State which parasite is depicted.
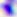
Toxoplasma gondii.

Summary:
  - Magnification: 400x
  - Modality: micrograph